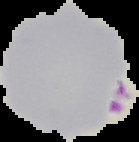

Summary:
  - Preparation: thin blood smear
  - Image type: segmented cell region with the area outside set to black
  - Malaria status: parasitized
  - Image size: 139×142 pixels